Locate every blood parasite and identify its species.
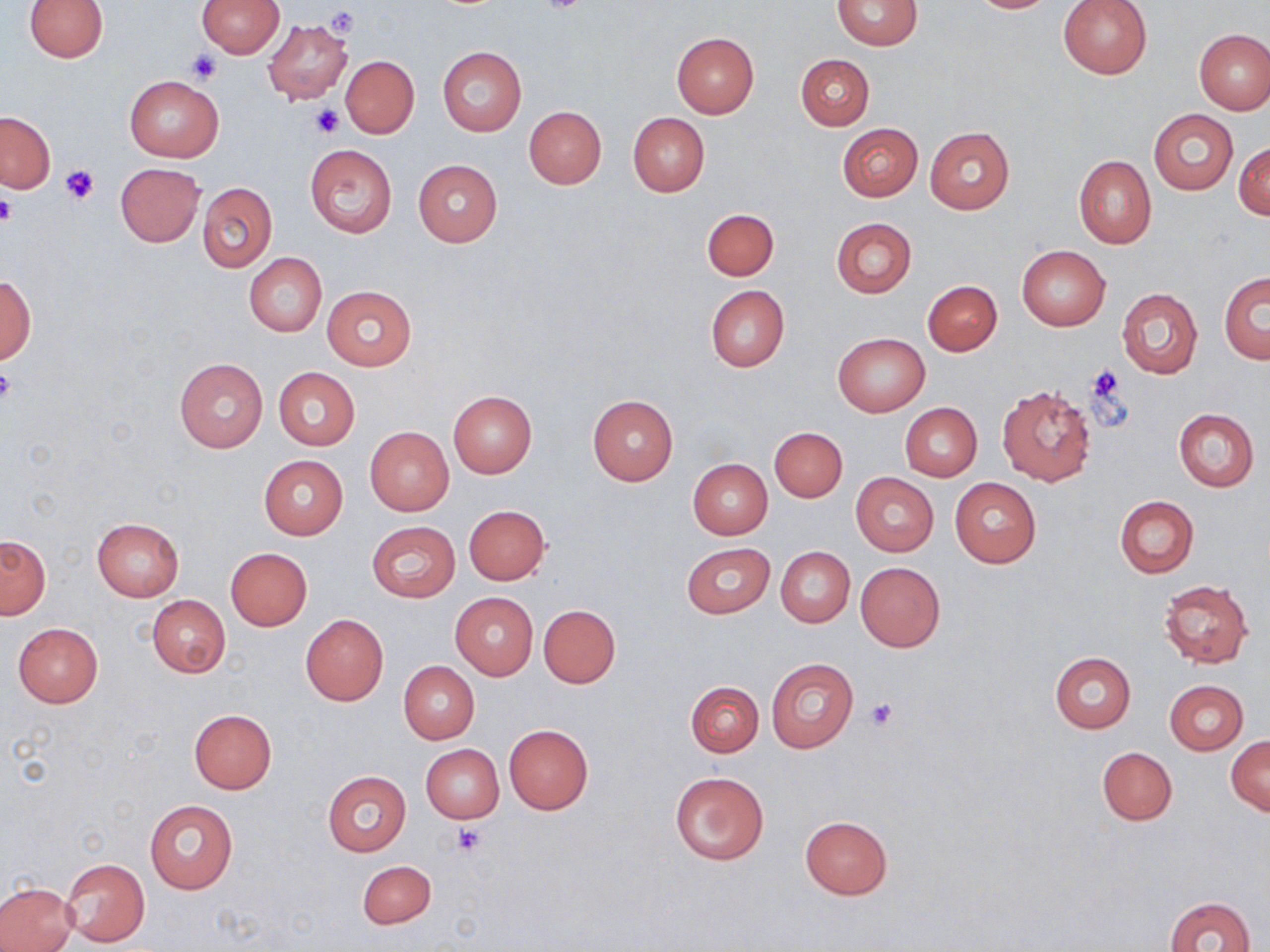
No blood parasites seen.

Approximate bounding boxes as named x1/y1/x2/y2 corners in pixels. Uninfected red blood cell locations: (x1=23, y1=0, x2=108, y2=62), (x1=196, y1=0, x2=285, y2=58), (x1=832, y1=0, x2=921, y2=50), (x1=967, y1=0, x2=1058, y2=13), (x1=1057, y1=0, x2=1153, y2=79), (x1=263, y1=20, x2=353, y2=104), (x1=1195, y1=28, x2=1270, y2=114), (x1=672, y1=32, x2=759, y2=118), (x1=437, y1=46, x2=526, y2=135), (x1=796, y1=54, x2=873, y2=129), (x1=340, y1=56, x2=419, y2=138), (x1=125, y1=76, x2=224, y2=161), (x1=524, y1=106, x2=605, y2=189), (x1=1149, y1=108, x2=1238, y2=195), (x1=0, y1=111, x2=55, y2=193), (x1=628, y1=113, x2=709, y2=197), (x1=836, y1=123, x2=922, y2=202), (x1=925, y1=126, x2=1015, y2=214), (x1=1234, y1=143, x2=1270, y2=220), (x1=305, y1=144, x2=397, y2=236), (x1=1073, y1=155, x2=1156, y2=248), (x1=413, y1=159, x2=503, y2=246), (x1=116, y1=163, x2=204, y2=246), (x1=197, y1=181, x2=277, y2=271), (x1=702, y1=208, x2=779, y2=280), (x1=830, y1=217, x2=916, y2=297), (x1=1017, y1=244, x2=1110, y2=330), (x1=243, y1=252, x2=327, y2=337), (x1=1219, y1=272, x2=1270, y2=363), (x1=0, y1=276, x2=35, y2=365), (x1=923, y1=280, x2=1001, y2=355), (x1=322, y1=285, x2=416, y2=370), (x1=705, y1=285, x2=790, y2=372), (x1=1117, y1=288, x2=1202, y2=378), (x1=832, y1=332, x2=930, y2=416), (x1=174, y1=358, x2=267, y2=453), (x1=272, y1=367, x2=360, y2=450), (x1=996, y1=383, x2=1097, y2=486), (x1=447, y1=391, x2=537, y2=478), (x1=587, y1=395, x2=678, y2=485), (x1=900, y1=403, x2=982, y2=481), (x1=1174, y1=408, x2=1258, y2=492), (x1=364, y1=426, x2=454, y2=516), (x1=769, y1=427, x2=847, y2=502), (x1=258, y1=456, x2=348, y2=539), (x1=687, y1=459, x2=773, y2=539), (x1=850, y1=472, x2=938, y2=556), (x1=949, y1=478, x2=1041, y2=568), (x1=1114, y1=495, x2=1199, y2=577), (x1=464, y1=505, x2=551, y2=586), (x1=91, y1=517, x2=184, y2=601), (x1=367, y1=521, x2=460, y2=602), (x1=1, y1=534, x2=50, y2=618), (x1=682, y1=542, x2=774, y2=618), (x1=776, y1=546, x2=855, y2=628), (x1=225, y1=547, x2=313, y2=630), (x1=855, y1=562, x2=945, y2=651), (x1=1158, y1=580, x2=1253, y2=666), (x1=450, y1=592, x2=538, y2=679), (x1=147, y1=595, x2=230, y2=678), (x1=538, y1=604, x2=621, y2=687), (x1=300, y1=614, x2=388, y2=706), (x1=12, y1=622, x2=104, y2=707), (x1=1049, y1=652, x2=1135, y2=733), (x1=765, y1=657, x2=859, y2=754), (x1=399, y1=662, x2=479, y2=743), (x1=686, y1=680, x2=762, y2=757), (x1=1164, y1=681, x2=1249, y2=754), (x1=189, y1=709, x2=277, y2=793), (x1=503, y1=724, x2=593, y2=813), (x1=1227, y1=734, x2=1270, y2=815), (x1=422, y1=745, x2=503, y2=822), (x1=1097, y1=746, x2=1177, y2=825), (x1=322, y1=771, x2=410, y2=856), (x1=669, y1=771, x2=769, y2=865), (x1=144, y1=799, x2=238, y2=894), (x1=800, y1=816, x2=892, y2=898), (x1=59, y1=857, x2=150, y2=946), (x1=357, y1=859, x2=436, y2=929), (x1=0, y1=882, x2=77, y2=951), (x1=1166, y1=895, x2=1256, y2=952). Platelet locations: (x1=534, y1=1, x2=592, y2=15), (x1=326, y1=7, x2=360, y2=37), (x1=186, y1=48, x2=223, y2=83), (x1=312, y1=104, x2=346, y2=138), (x1=59, y1=165, x2=100, y2=204), (x1=0, y1=192, x2=16, y2=227), (x1=1086, y1=366, x2=1131, y2=424), (x1=0, y1=367, x2=16, y2=408), (x1=866, y1=698, x2=896, y2=730), (x1=451, y1=824, x2=485, y2=855). Slide-level diagnosis: no evidence of blood parasites. One field of a larger specimen. Image is 1270×952 pixels. May-Grünwald-Giemsa stain. Thin blood smear. Captured at 1000x magnification. Light microscopy.